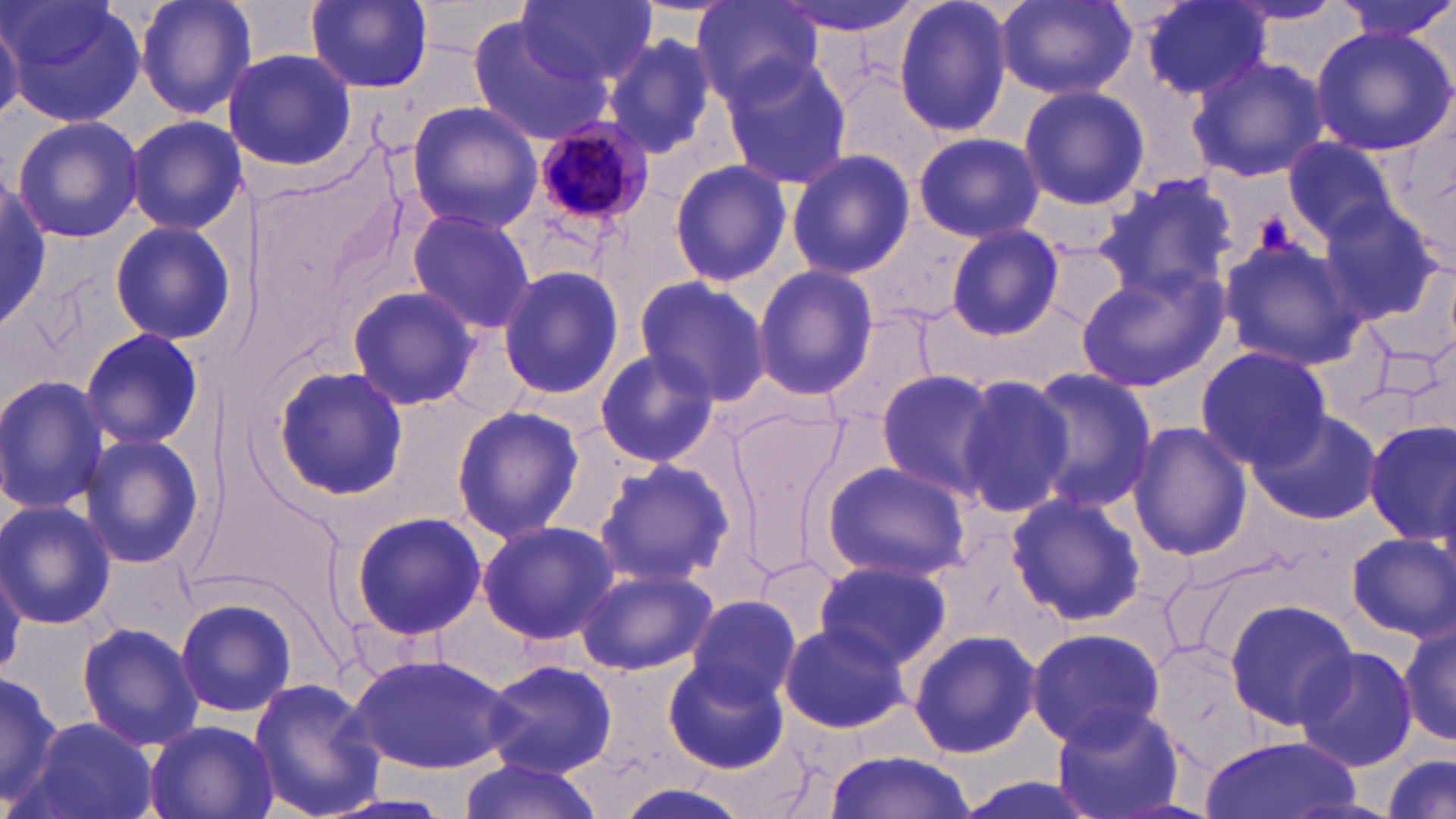
Summary:
  - Coordinate format: approximate bounding boxes as [x1, y1, x2, y2] in pixels
  - Plasmodium malariae-infected red blood cell locations: [530, 121, 656, 229]
  - Uninfected red blood cell locations: [3, 0, 147, 130], [134, 0, 257, 121], [305, 0, 433, 91], [519, 0, 658, 86], [690, 0, 824, 107], [774, 0, 930, 38], [894, 0, 1015, 139], [996, 0, 1136, 101], [1136, 0, 1272, 102], [1333, 0, 1456, 45], [0, 11, 23, 124], [464, 11, 614, 144], [1309, 26, 1454, 157], [601, 30, 724, 162], [227, 48, 357, 170], [1187, 55, 1327, 183], [721, 56, 853, 192], [1017, 84, 1150, 210], [405, 100, 545, 233], [125, 114, 244, 237], [11, 115, 146, 243], [911, 130, 1044, 242], [1281, 136, 1397, 243], [786, 150, 915, 281], [668, 160, 793, 287], [0, 174, 47, 331], [1095, 174, 1240, 302], [1313, 201, 1442, 323], [404, 209, 536, 334], [106, 218, 234, 348], [945, 224, 1065, 339], [1217, 236, 1364, 372], [752, 265, 878, 399], [1073, 265, 1227, 390], [496, 266, 625, 399], [632, 276, 772, 409], [347, 285, 480, 412], [822, 311, 942, 439], [78, 328, 206, 449], [1195, 348, 1331, 467], [594, 349, 720, 467], [268, 364, 409, 502], [873, 369, 998, 496], [1015, 369, 1156, 514], [952, 374, 1072, 514], [0, 377, 112, 514], [450, 406, 585, 542], [1247, 408, 1384, 525], [1364, 420, 1456, 544], [1128, 423, 1252, 561], [77, 434, 203, 569], [593, 458, 737, 589], [820, 460, 970, 580], [1005, 491, 1144, 626], [0, 501, 116, 630], [347, 511, 486, 642], [477, 520, 620, 646], [1347, 534, 1456, 640], [756, 554, 844, 647], [813, 559, 951, 671], [573, 566, 717, 676], [685, 593, 802, 707], [174, 595, 299, 719], [1225, 598, 1357, 729], [1397, 613, 1453, 748], [77, 621, 203, 751], [778, 622, 911, 734], [1026, 626, 1165, 748], [907, 627, 1042, 758], [1294, 645, 1418, 771], [347, 653, 516, 775], [663, 655, 789, 773], [481, 658, 618, 778], [0, 676, 64, 811], [248, 678, 385, 819], [1049, 701, 1185, 819], [25, 717, 158, 819], [143, 720, 277, 819], [1200, 735, 1364, 819], [823, 751, 976, 819], [1379, 753, 1454, 819], [457, 757, 607, 818], [951, 775, 1103, 819], [610, 783, 753, 819]
  - Slide-level diagnosis: Plasmodium malariae
  - Preparation: thin blood smear
  - Field of view: single
  - Stain: May-Grünwald-Giemsa
  - Magnification: 1000x
  - Image size: 1456×819 pixels
  - Modality: light microscopy